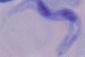
modality = photomicrograph
magnification = 1000x
identification = trypanosome